Classify this cell by malaria status.
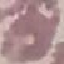
It is uninfected.

Photographed with a smartphone camera at the microscope eyepiece. Cell patch, automatically extracted from a larger field of view and resized to 64 × 64 pixels. Thin blood film. Giemsa-stained preparation.